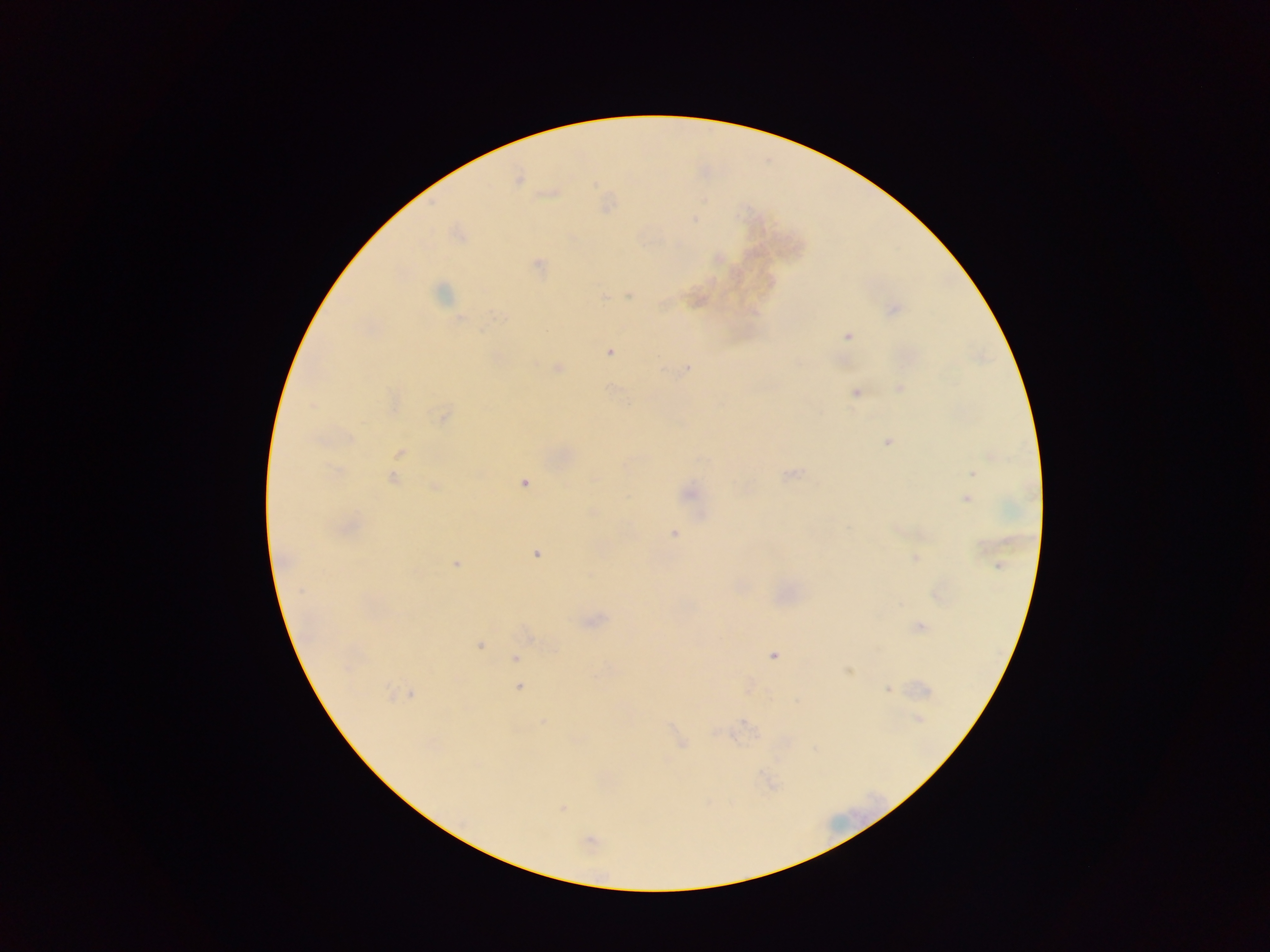

country = Ghana
field of view = single
image size = 1270×952 pixels
capture = mobile-phone photograph through a microscope
Plasmodium parasite locations = approximate centers as (x, y) in pixels: (518, 179), (694, 218), (459, 234), (718, 258), (538, 265), (441, 293), (629, 295), (697, 300), (891, 309), (848, 336), (608, 352), (557, 368), (687, 369), (900, 388), (855, 391), (394, 402), (442, 415), (887, 440), (399, 453), (973, 473), (790, 474), (392, 477), (523, 482), (436, 487), (689, 493), (966, 498), (345, 527), (674, 534), (536, 553), (916, 558), (455, 564), (937, 593), (592, 620), (919, 627), (479, 645), (774, 654), (516, 659), (847, 670), (518, 686), (749, 687), (888, 690), (402, 694), (917, 720), (543, 722), (680, 742), (562, 807), (589, 841)
preparation = thick blood smear